State which parasite is depicted.
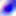

Toxoplasma gondii.

magnification = 400x
modality = photomicrograph